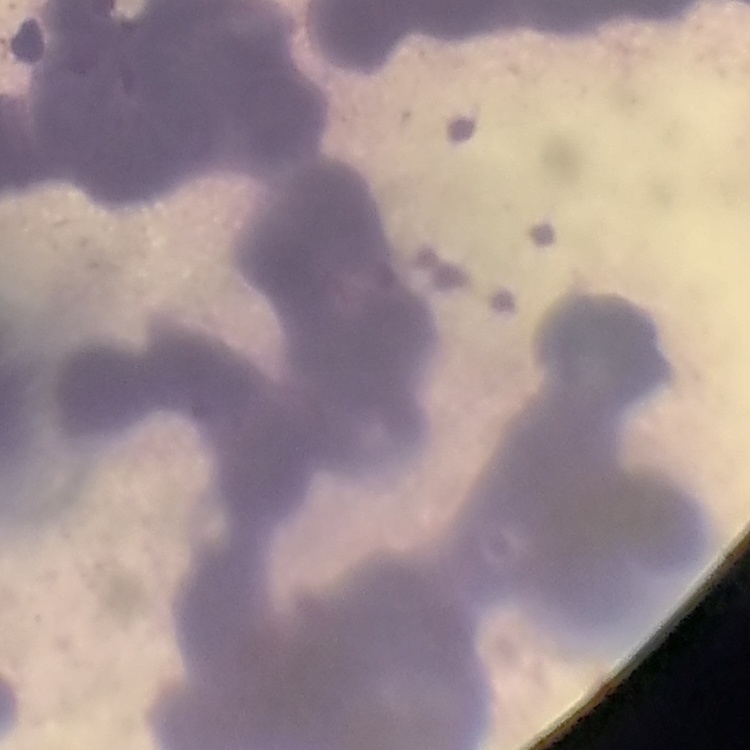 The erythrocytes exhibit rouleaux formation. Field's or Giemsa stain. Thin peripheral smear. One tile cut from a larger photomicrograph.